Give the extent of all uninfected red blood cells.
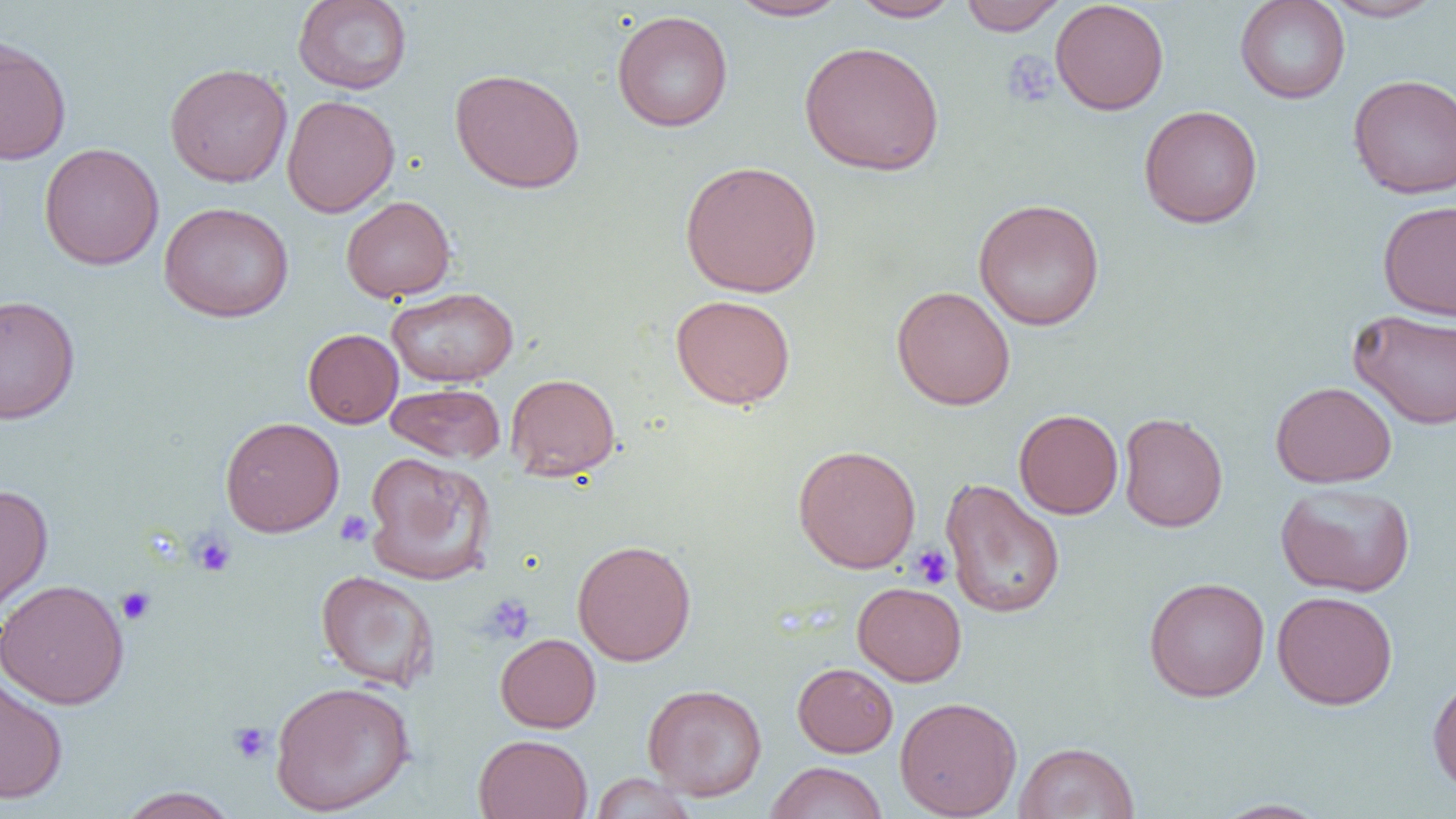
Approximate bounding boxes as (x1, y1, x2, y2) in pixels.
Uninfected red blood cells: (293, 0, 412, 95), (727, 0, 850, 21), (851, 0, 963, 22), (959, 0, 1067, 35), (1050, 0, 1169, 115), (1235, 0, 1350, 104), (1322, 1, 1445, 22), (612, 9, 733, 132), (0, 35, 72, 165), (798, 40, 945, 176), (164, 62, 293, 187), (449, 68, 585, 193), (1348, 73, 1456, 199), (281, 95, 400, 217), (1138, 104, 1263, 228), (39, 142, 164, 270), (679, 159, 823, 298), (340, 196, 456, 302), (973, 198, 1105, 331), (1377, 200, 1456, 321), (158, 201, 294, 323), (891, 285, 1016, 411), (387, 286, 518, 387), (0, 294, 80, 424), (670, 294, 796, 409), (1349, 309, 1456, 430), (303, 328, 403, 428), (505, 373, 621, 480), (1270, 381, 1397, 488), (385, 383, 505, 463), (370, 396, 501, 536), (1014, 409, 1123, 519), (1118, 412, 1228, 532), (220, 416, 344, 537), (793, 443, 922, 574), (362, 451, 495, 585), (940, 478, 1066, 619), (1275, 482, 1415, 598), (0, 483, 53, 614), (572, 539, 696, 666), (315, 570, 439, 691), (1143, 577, 1270, 702), (0, 579, 129, 709), (852, 581, 967, 686), (1271, 590, 1398, 709), (495, 633, 601, 732), (792, 662, 898, 757), (1427, 671, 1456, 795), (0, 673, 69, 804), (269, 680, 415, 816), (642, 683, 767, 801), (894, 696, 1022, 819), (473, 733, 593, 819), (1014, 741, 1140, 819), (764, 761, 888, 819), (589, 773, 698, 818), (116, 787, 240, 818), (1211, 798, 1333, 818).

Platelet locations: (1000, 50, 1058, 108), (335, 510, 374, 547), (190, 532, 236, 577), (911, 544, 954, 588), (116, 586, 156, 625), (481, 595, 535, 644), (228, 721, 272, 764). Slide-level diagnosis: negative for blood parasites. 1000x magnification. Single field of view. Image is 1456×819 pixels. Optical microscopy. Thin blood smear.